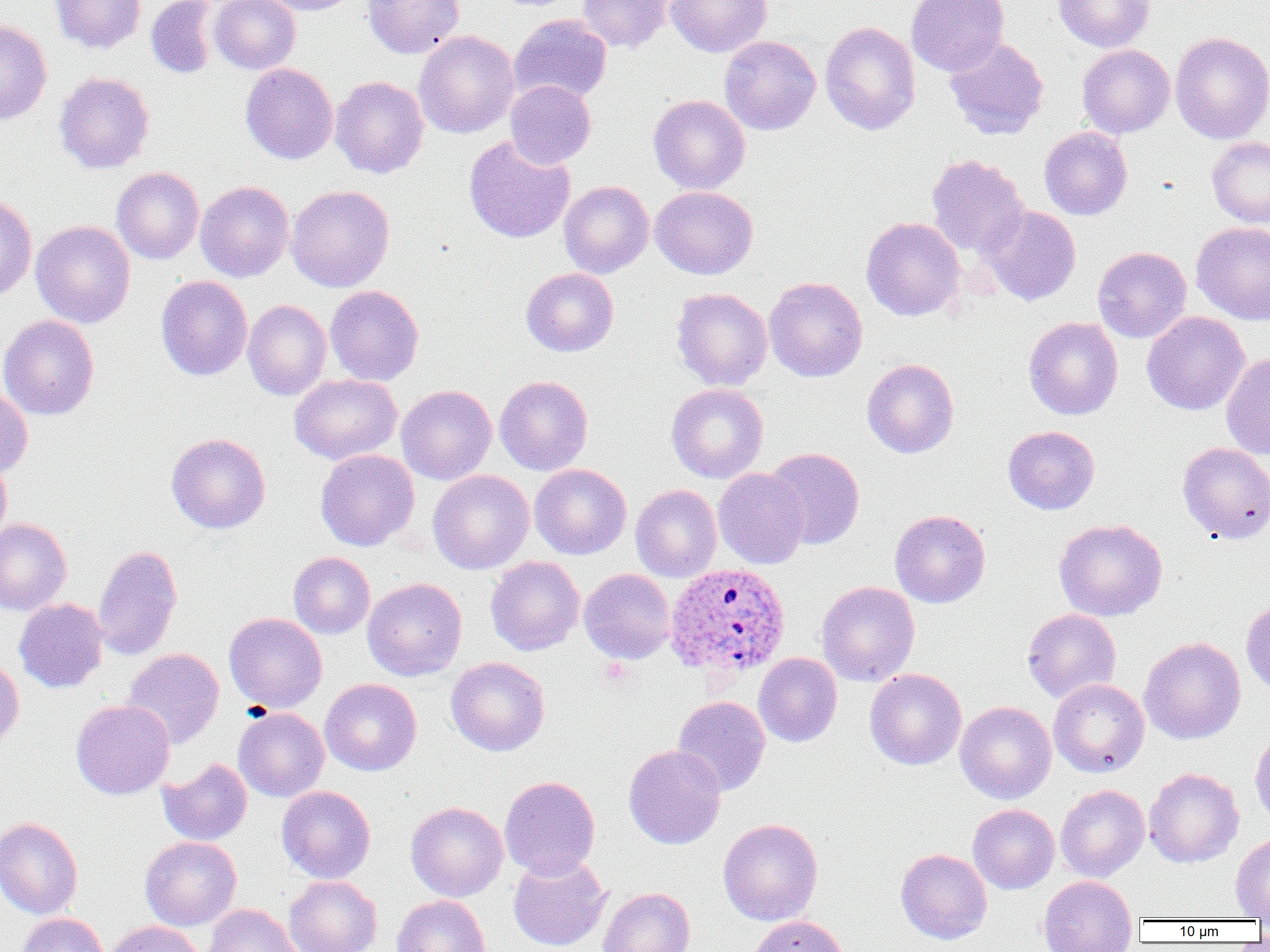

slide-level diagnosis = Plasmodium ovale
magnification = 1000x
modality = light microscopy
preparation = thin blood smear
Plasmodium ovale-infected red blood cell locations = approximate bounding boxes as named x1/y1/x2/y2 corners in pixels: (x1=664, y1=562, x2=790, y2=680)
image size = 1270×952 pixels
field of view = single
uninfected red blood cell locations = approximate bounding boxes as named x1/y1/x2/y2 corners in pixels: (x1=50, y1=0, x2=146, y2=54), (x1=145, y1=0, x2=218, y2=79), (x1=210, y1=0, x2=301, y2=75), (x1=254, y1=0, x2=365, y2=15), (x1=362, y1=0, x2=465, y2=59), (x1=577, y1=0, x2=675, y2=53), (x1=665, y1=0, x2=772, y2=58), (x1=906, y1=0, x2=1009, y2=77), (x1=1053, y1=0, x2=1156, y2=52), (x1=509, y1=14, x2=612, y2=104), (x1=0, y1=20, x2=52, y2=125), (x1=819, y1=21, x2=921, y2=136), (x1=414, y1=30, x2=520, y2=139), (x1=1170, y1=31, x2=1270, y2=144), (x1=719, y1=35, x2=820, y2=135), (x1=944, y1=37, x2=1049, y2=139), (x1=1077, y1=44, x2=1175, y2=139), (x1=240, y1=63, x2=338, y2=164), (x1=54, y1=71, x2=155, y2=174), (x1=331, y1=76, x2=430, y2=178), (x1=505, y1=80, x2=596, y2=168), (x1=648, y1=95, x2=750, y2=194), (x1=1039, y1=127, x2=1132, y2=220), (x1=463, y1=134, x2=575, y2=244), (x1=1207, y1=136, x2=1270, y2=228), (x1=926, y1=154, x2=1029, y2=259), (x1=112, y1=167, x2=204, y2=265), (x1=195, y1=180, x2=295, y2=282), (x1=559, y1=180, x2=654, y2=279), (x1=286, y1=185, x2=395, y2=292), (x1=650, y1=186, x2=759, y2=279), (x1=0, y1=194, x2=37, y2=301), (x1=982, y1=205, x2=1081, y2=306), (x1=861, y1=217, x2=965, y2=321), (x1=31, y1=220, x2=136, y2=328), (x1=1191, y1=221, x2=1270, y2=326), (x1=1092, y1=246, x2=1192, y2=343), (x1=521, y1=268, x2=618, y2=357), (x1=156, y1=275, x2=253, y2=381), (x1=764, y1=277, x2=868, y2=382), (x1=325, y1=284, x2=424, y2=386), (x1=671, y1=287, x2=772, y2=390), (x1=243, y1=299, x2=332, y2=400), (x1=1142, y1=311, x2=1250, y2=416), (x1=0, y1=315, x2=100, y2=420), (x1=1023, y1=317, x2=1123, y2=420), (x1=1221, y1=353, x2=1270, y2=460), (x1=862, y1=358, x2=959, y2=459), (x1=289, y1=374, x2=402, y2=465), (x1=494, y1=375, x2=593, y2=476), (x1=666, y1=383, x2=769, y2=483), (x1=396, y1=384, x2=497, y2=485), (x1=0, y1=385, x2=33, y2=479), (x1=1003, y1=425, x2=1100, y2=515), (x1=166, y1=432, x2=271, y2=534), (x1=1178, y1=442, x2=1270, y2=543), (x1=764, y1=447, x2=865, y2=549), (x1=315, y1=448, x2=420, y2=551), (x1=0, y1=456, x2=12, y2=545), (x1=529, y1=463, x2=632, y2=560), (x1=713, y1=468, x2=809, y2=569), (x1=428, y1=470, x2=535, y2=575), (x1=631, y1=484, x2=722, y2=582), (x1=890, y1=510, x2=990, y2=608), (x1=0, y1=518, x2=72, y2=616), (x1=1054, y1=518, x2=1167, y2=621), (x1=92, y1=544, x2=183, y2=661), (x1=288, y1=551, x2=375, y2=639), (x1=485, y1=556, x2=585, y2=656), (x1=579, y1=568, x2=675, y2=664), (x1=362, y1=577, x2=467, y2=681), (x1=816, y1=581, x2=920, y2=686), (x1=1241, y1=598, x2=1270, y2=697), (x1=13, y1=599, x2=108, y2=693), (x1=1022, y1=608, x2=1121, y2=704), (x1=225, y1=612, x2=327, y2=713), (x1=1139, y1=636, x2=1246, y2=745), (x1=122, y1=648, x2=224, y2=749), (x1=753, y1=653, x2=842, y2=747), (x1=0, y1=656, x2=24, y2=748), (x1=446, y1=656, x2=550, y2=756), (x1=864, y1=668, x2=966, y2=770), (x1=320, y1=678, x2=422, y2=776), (x1=1048, y1=678, x2=1149, y2=777), (x1=672, y1=696, x2=770, y2=796), (x1=71, y1=699, x2=175, y2=799), (x1=955, y1=701, x2=1056, y2=803), (x1=234, y1=707, x2=329, y2=801), (x1=1249, y1=731, x2=1270, y2=830), (x1=623, y1=744, x2=726, y2=850), (x1=158, y1=758, x2=253, y2=846), (x1=1144, y1=767, x2=1244, y2=867), (x1=499, y1=775, x2=600, y2=880), (x1=1055, y1=784, x2=1150, y2=882), (x1=276, y1=785, x2=376, y2=883), (x1=406, y1=801, x2=508, y2=901), (x1=968, y1=804, x2=1059, y2=894), (x1=0, y1=817, x2=83, y2=919), (x1=718, y1=818, x2=823, y2=926), (x1=1230, y1=834, x2=1270, y2=920), (x1=140, y1=836, x2=241, y2=930), (x1=896, y1=848, x2=992, y2=944), (x1=508, y1=853, x2=610, y2=951), (x1=284, y1=875, x2=382, y2=952), (x1=1038, y1=875, x2=1137, y2=951), (x1=598, y1=887, x2=695, y2=952), (x1=392, y1=894, x2=490, y2=952), (x1=203, y1=904, x2=304, y2=952), (x1=17, y1=913, x2=108, y2=952), (x1=748, y1=915, x2=849, y2=952), (x1=104, y1=920, x2=205, y2=952)